Outline each blood parasite and name the species.
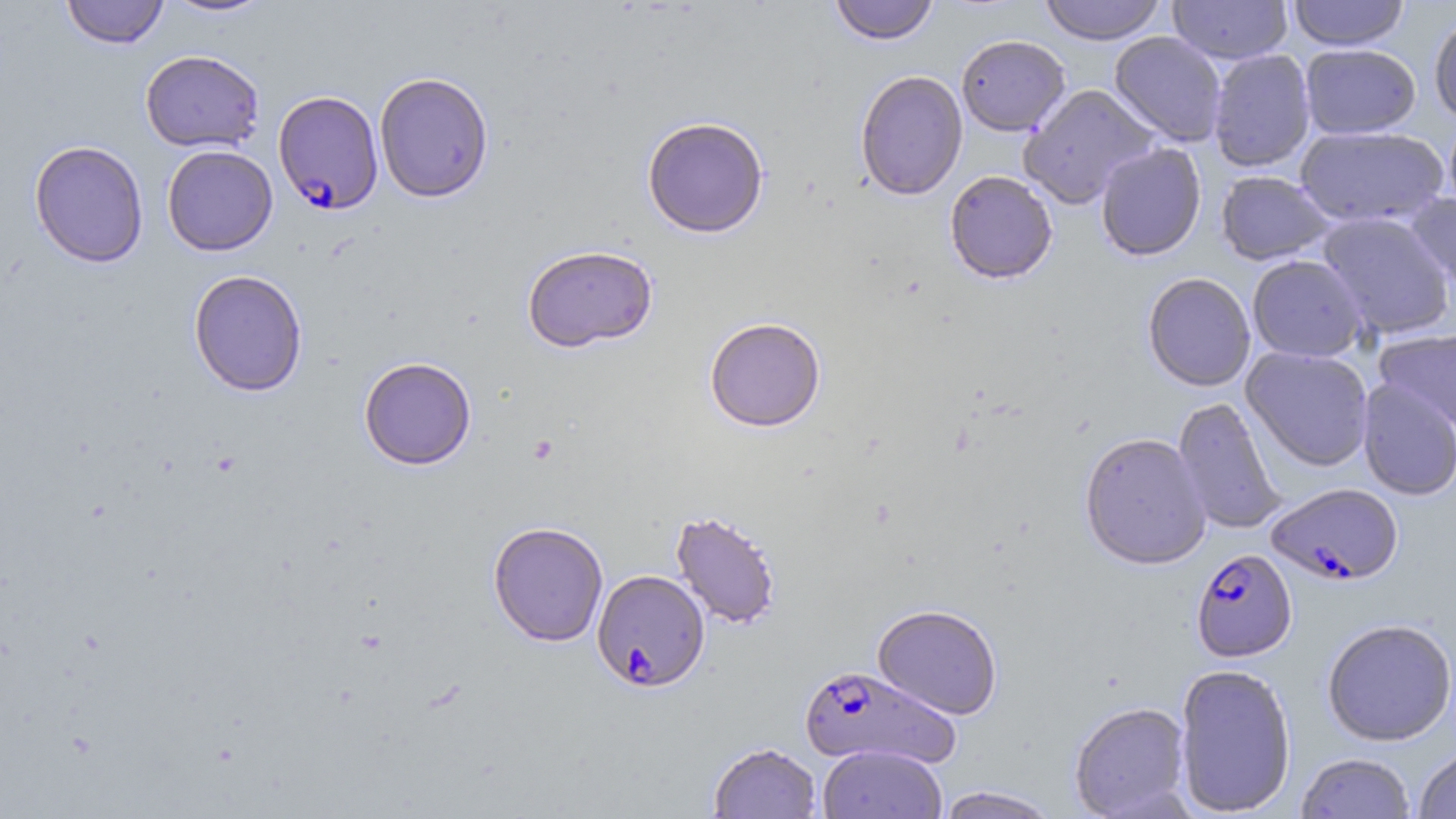

Approximate bounding boxes as (x1,y1)-(x2,y2) corner pairs in pixels.
Plasmodium falciparum-infected red blood cells: (273,90)-(384,214), (1266,483)-(1404,586), (1191,549)-(1297,663), (591,569)-(710,692), (798,665)-(961,770).
No Plasmodium ovale, Plasmodium malariae, Plasmodium vivax, Babesia divergens, or Trypanosoma brucei observed.

{
  "slide_level_diagnosis": "Plasmodium falciparum",
  "magnification": "1000x",
  "stain": "May-Grünwald-Giemsa",
  "uninfected_red_blood_cell_locations": "approximate bounding boxes as (x1,y1)-(x2,y2) corner pairs in pixels: (61,0)-(169,49), (162,0)-(275,19), (828,0)-(939,46), (1039,0)-(1168,45), (1168,0)-(1293,64), (1287,0)-(1410,51), (1428,12)-(1456,126), (1109,31)-(1227,147), (955,34)-(1071,136), (1300,44)-(1421,140), (139,49)-(265,153), (1208,49)-(1316,173), (854,70)-(968,201), (374,72)-(494,203), (1018,84)-(1160,210), (1443,113)-(1456,217), (642,117)-(769,238), (1294,125)-(1449,228), (28,139)-(149,268), (1095,143)-(1207,262), (162,144)-(278,256), (944,171)-(1058,285), (1216,171)-(1336,265), (1404,192)-(1456,300), (1316,212)-(1456,340), (522,245)-(658,353), (1247,255)-(1369,362), (188,269)-(308,397), (1142,272)-(1256,391), (704,317)-(826,432), (1374,328)-(1456,434), (1241,346)-(1375,472), (358,356)-(477,470), (1357,379)-(1455,501), (1171,397)-(1288,535), (1079,432)-(1212,570), (670,510)-(782,630), (488,520)-(609,646), (872,603)-(1003,720), (1321,618)-(1456,746), (1174,663)-(1296,817), (1068,701)-(1192,818), (707,742)-(822,819), (818,744)-(947,819), (1413,746)-(1456,818), (1295,753)-(1416,818), (935,786)-(1061,818)",
  "image_size": "1456×819 pixels",
  "modality": "light microscopy",
  "field_of_view": "single",
  "preparation": "thin blood film"
}